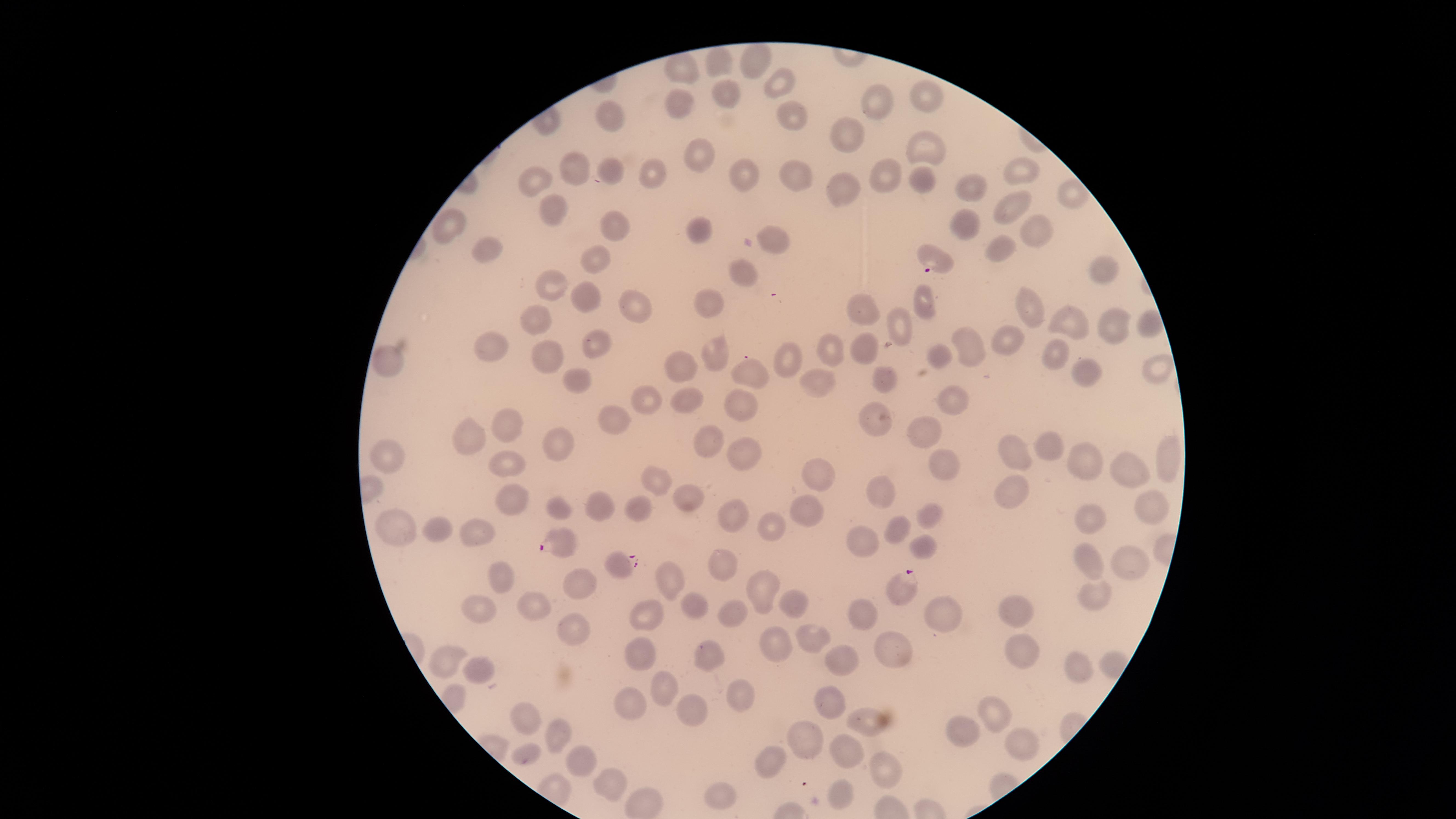

Approximate marker points as [x, y] in pixels.
Summary:
  - Uninfected RBCs: [757, 63], [720, 64], [678, 70], [778, 80], [925, 91], [727, 94], [883, 102], [675, 110], [792, 114], [610, 115], [856, 137], [927, 146], [702, 156], [581, 166], [610, 167], [1020, 172], [746, 173], [891, 174], [800, 175], [659, 176], [922, 177], [541, 179], [842, 186], [974, 187], [1071, 197], [549, 207], [1013, 207], [966, 220], [450, 224], [611, 225], [1037, 225], [695, 232], [778, 240], [1003, 247], [483, 251], [598, 261], [749, 271], [1101, 274], [557, 284], [584, 295], [713, 304], [926, 304], [643, 307], [863, 309], [1035, 309], [898, 320], [535, 321], [1061, 323], [1140, 324], [1109, 327], [1002, 337], [965, 341], [597, 342], [496, 343], [828, 346], [868, 347], [720, 350], [1055, 351], [782, 353], [544, 354], [936, 354], [687, 361], [393, 362], [1083, 365], [1155, 367], [750, 372], [570, 374], [813, 376], [888, 379], [647, 394], [685, 398], [949, 402], [739, 407], [619, 416], [871, 420], [507, 426], [472, 438], [929, 438], [555, 442], [708, 443], [1057, 446], [1014, 449], [751, 451], [389, 453], [945, 457], [1087, 459], [499, 463], [1166, 465], [817, 468], [1130, 469], [659, 480], [885, 489], [1007, 492], [514, 496], [686, 501], [597, 505], [561, 508], [811, 508], [1155, 508], [644, 512], [734, 515], [1087, 516], [928, 517], [435, 524], [396, 527], [773, 527], [482, 530], [894, 532], [864, 542], [921, 543], [724, 554], [1134, 562], [1088, 563], [573, 577], [498, 579], [664, 580], [768, 587], [1093, 597], [794, 601], [536, 604], [696, 604], [729, 608], [943, 610], [476, 612], [1019, 615], [650, 616], [862, 616], [573, 634], [811, 635], [776, 639], [709, 653], [897, 653], [646, 656], [1026, 656], [1075, 660], [447, 661], [847, 661], [478, 667], [733, 686], [663, 688], [835, 697], [629, 701], [696, 710], [991, 714], [525, 715], [860, 718], [968, 731], [559, 733], [810, 738], [1018, 739], [530, 751], [850, 753], [586, 760], [768, 761], [889, 770], [612, 781], [835, 791], [726, 794]
  - Parasitized RBCs: [937, 262], [564, 540], [619, 566], [903, 584]
  - Stain: Giemsa
  - Species: Plasmodium falciparum
  - Field of view: single
  - Capture: smartphone photograph through the microscope eyepiece
  - Visible region: circular
  - Presence: malaria parasites identified
  - Image size: 1456×819 pixels
  - Preparation: thin smear of blood